Locate every leukocyte (white blood cell).
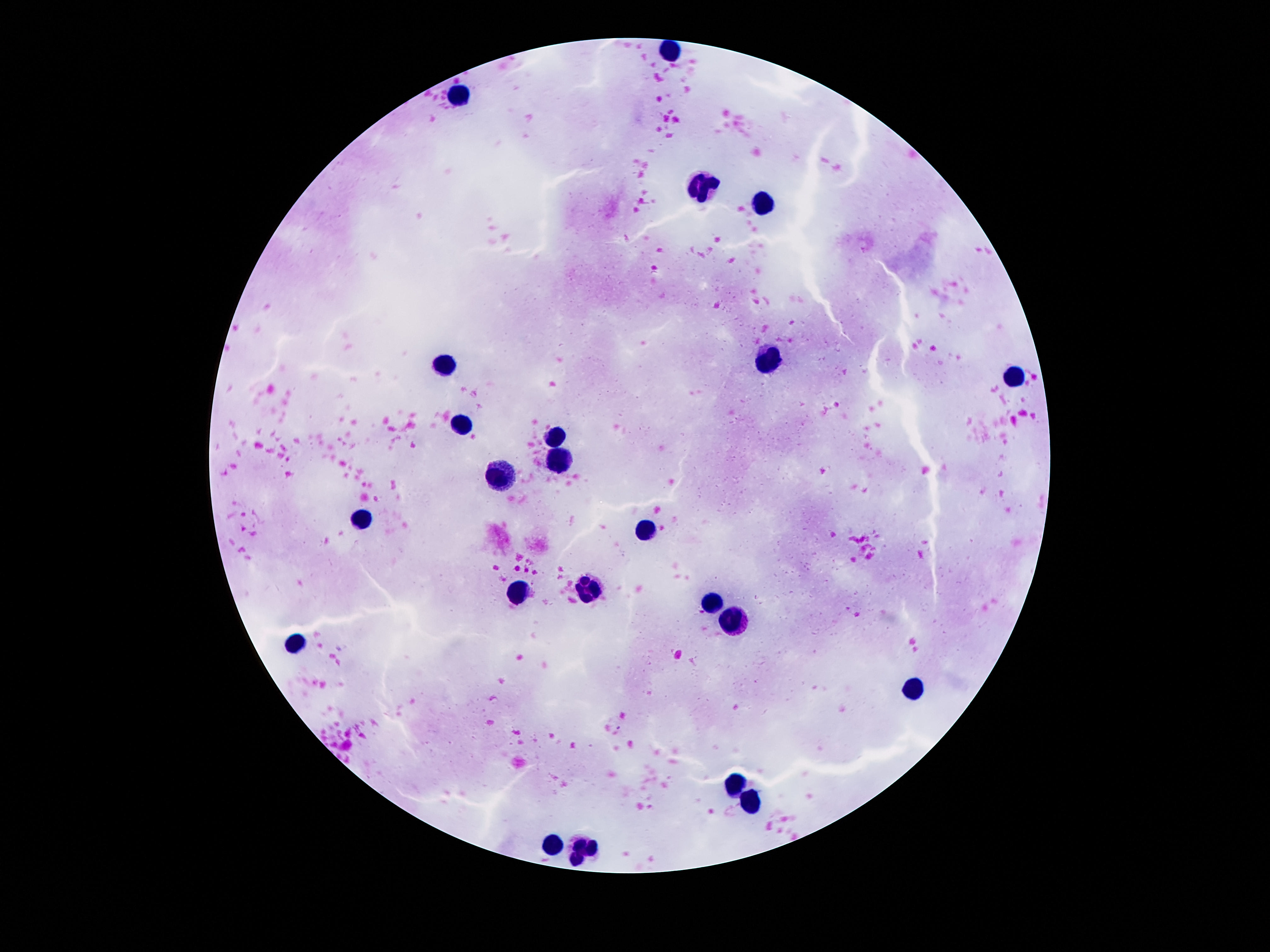
Approximate centers as {x, y} in pixels.
Leukocytes: {669, 48}, {457, 96}, {704, 188}, {763, 207}, {772, 361}, {445, 363}, {1019, 375}, {459, 428}, {555, 435}, {558, 458}, {499, 480}, {361, 517}, {642, 529}, {585, 590}, {516, 594}, {709, 606}, {728, 618}, {296, 644}, {912, 690}, {737, 787}, {756, 802}, {555, 844}, {583, 851}.

{
  "image_size": "1270×952 pixels",
  "magnification": "100x",
  "patient_malaria_status": "not infected",
  "preparation": "thick blood smear",
  "capture": "smartphone camera through the microscope eyepiece",
  "stain": "Giemsa",
  "field_of_view": "one from this slide"
}